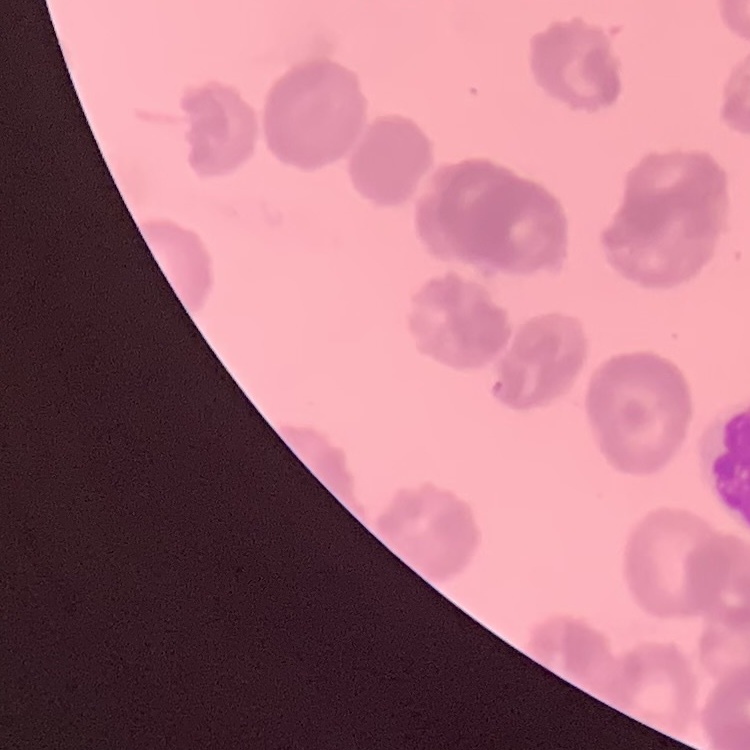

red blood cell morphology = rouleaux formation
stain = Field's or Giemsa
preparation = thin peripheral smear
image type = square crop of a larger photomicrograph